Assess this cell for malaria.
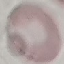

It is uninfected.

{
  "image_type": "cell patch, automatically extracted from a larger field of view and resized to 64 × 64 pixels",
  "stain": "Giemsa",
  "capture": "smartphone camera at the microscope eyepiece",
  "preparation": "thin blood smear"
}